Assess the morphology of the red blood cells.
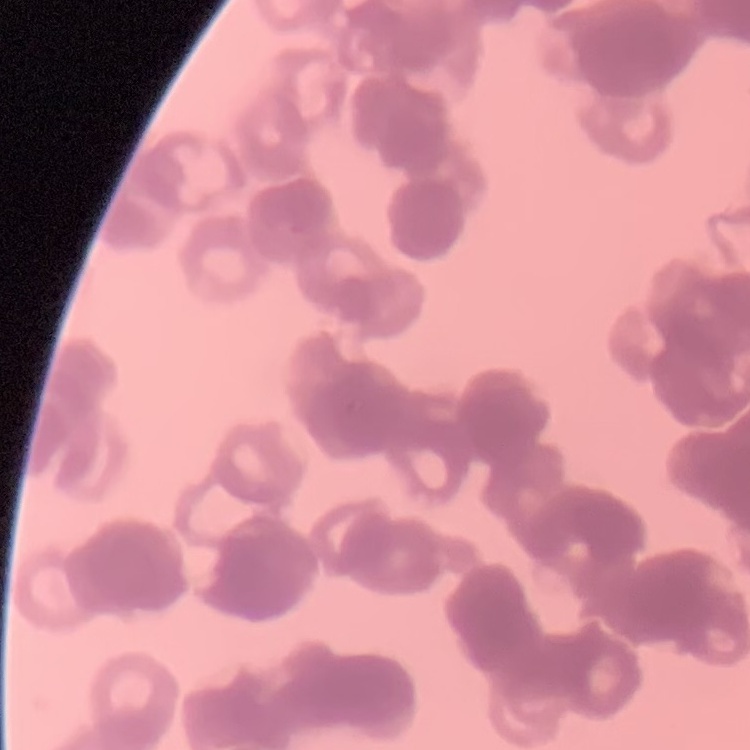
Rouleaux formation.

Thin blood film. Field's or Giemsa stain. One tile cut from a larger photomicrograph.